Describe the morphology of the erythrocytes.
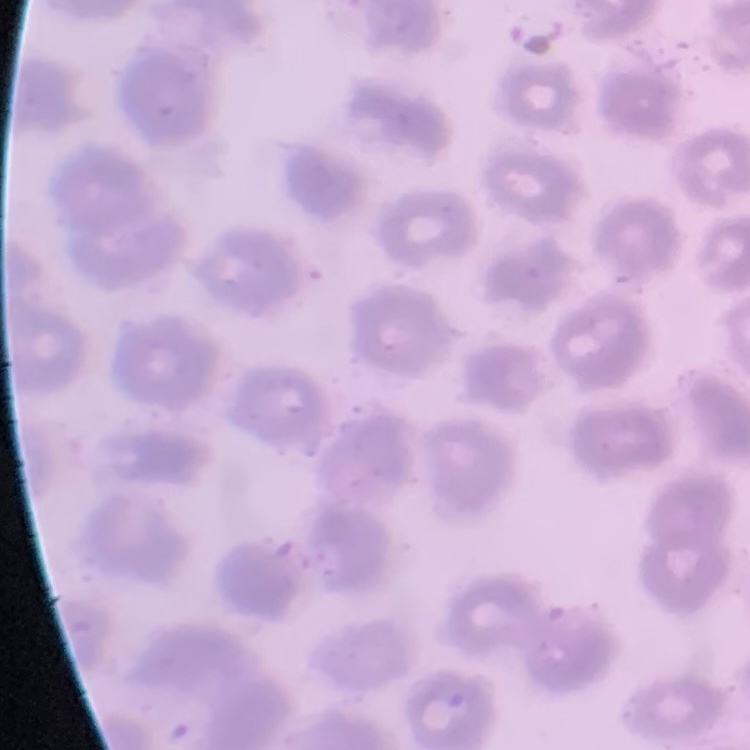

No rouleaux formation.

Square crop of a larger photomicrograph. Thin blood smear. Stained with either Field's or Giemsa.